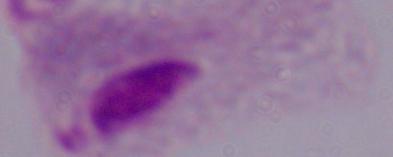

Summary:
  - Identification: trichomonad
  - Modality: photomicrograph
  - Magnification: 1000x